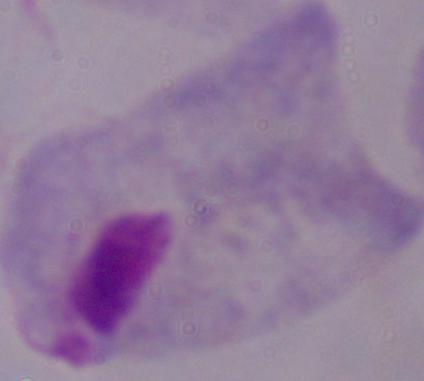
A trichomonad is shown. Photomicrograph. Captured at 1000x magnification.